Outline each uninfected red blood cell.
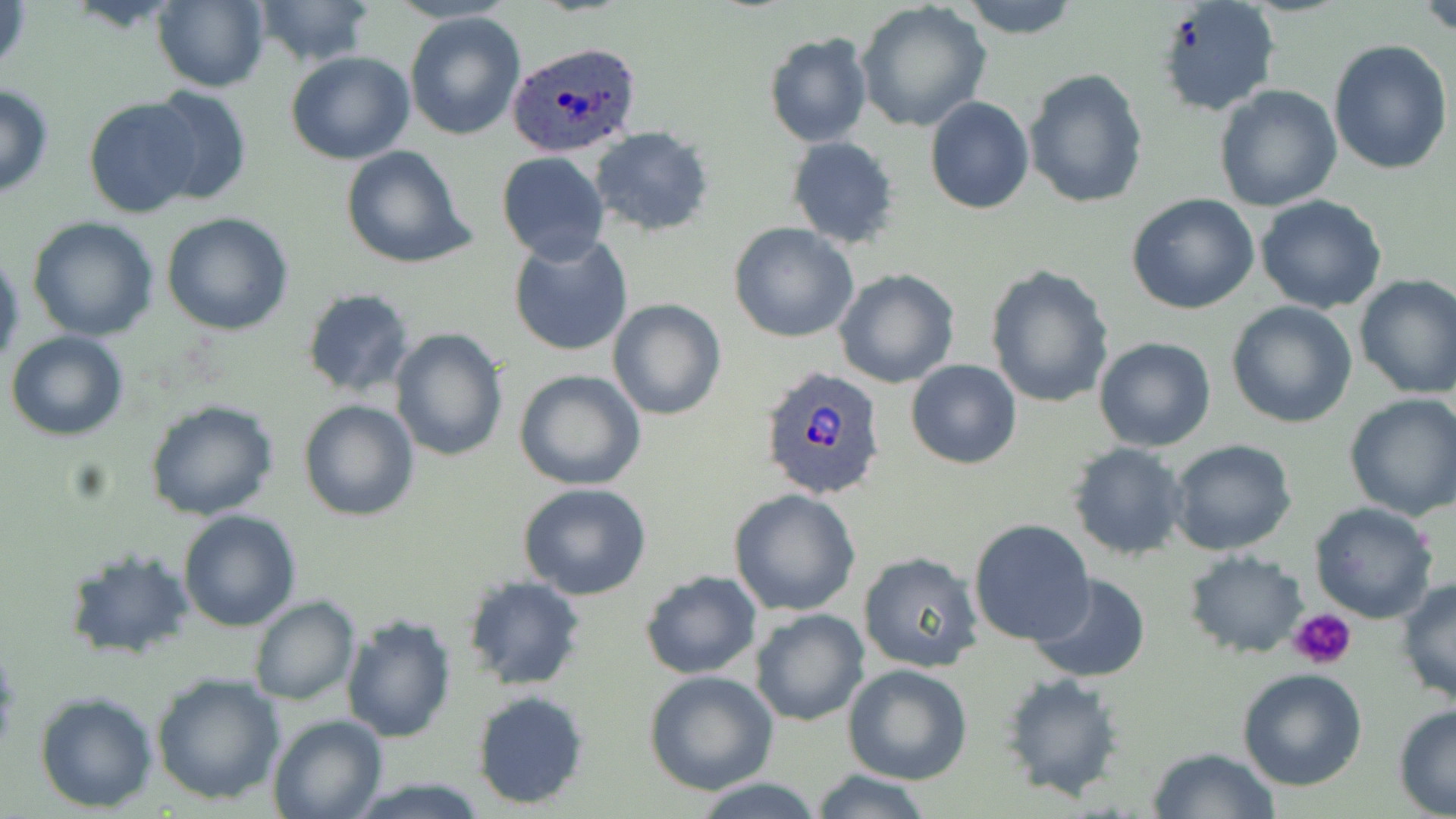

Approximate bounding boxes as named x1/y1/x2/y2 corners in pixels.
Uninfected red blood cells: (x1=1, y1=0, x2=32, y2=82), (x1=152, y1=0, x2=270, y2=92), (x1=956, y1=0, x2=1083, y2=38), (x1=1155, y1=0, x2=1280, y2=115), (x1=1417, y1=0, x2=1456, y2=36), (x1=252, y1=2, x2=375, y2=66), (x1=857, y1=3, x2=992, y2=134), (x1=402, y1=12, x2=526, y2=141), (x1=763, y1=32, x2=874, y2=148), (x1=1328, y1=38, x2=1452, y2=175), (x1=285, y1=51, x2=415, y2=165), (x1=1023, y1=69, x2=1149, y2=210), (x1=0, y1=82, x2=54, y2=199), (x1=1214, y1=84, x2=1343, y2=212), (x1=144, y1=85, x2=252, y2=205), (x1=83, y1=96, x2=204, y2=219), (x1=924, y1=97, x2=1034, y2=215), (x1=588, y1=127, x2=713, y2=238), (x1=786, y1=136, x2=902, y2=250), (x1=340, y1=145, x2=476, y2=270), (x1=496, y1=151, x2=611, y2=264), (x1=1125, y1=192, x2=1261, y2=315), (x1=1254, y1=194, x2=1388, y2=314), (x1=161, y1=211, x2=294, y2=335), (x1=27, y1=217, x2=160, y2=341), (x1=729, y1=223, x2=860, y2=344), (x1=507, y1=234, x2=633, y2=357), (x1=0, y1=249, x2=23, y2=369), (x1=984, y1=264, x2=1115, y2=408), (x1=834, y1=270, x2=960, y2=388), (x1=1353, y1=274, x2=1456, y2=398), (x1=300, y1=288, x2=416, y2=397), (x1=607, y1=299, x2=727, y2=420), (x1=1226, y1=300, x2=1358, y2=428), (x1=388, y1=328, x2=509, y2=463), (x1=6, y1=329, x2=129, y2=441), (x1=1094, y1=337, x2=1218, y2=452), (x1=906, y1=359, x2=1023, y2=469), (x1=513, y1=369, x2=646, y2=491), (x1=1343, y1=393, x2=1456, y2=521), (x1=144, y1=397, x2=279, y2=521), (x1=298, y1=399, x2=420, y2=520), (x1=1167, y1=439, x2=1297, y2=556), (x1=1066, y1=442, x2=1189, y2=562), (x1=518, y1=482, x2=654, y2=601), (x1=729, y1=488, x2=860, y2=616), (x1=1308, y1=502, x2=1439, y2=624), (x1=178, y1=509, x2=302, y2=631), (x1=968, y1=518, x2=1094, y2=644), (x1=66, y1=545, x2=194, y2=661), (x1=1184, y1=550, x2=1309, y2=659), (x1=858, y1=552, x2=984, y2=674), (x1=639, y1=570, x2=763, y2=679), (x1=461, y1=574, x2=588, y2=689), (x1=1026, y1=574, x2=1151, y2=683), (x1=1396, y1=576, x2=1456, y2=709), (x1=249, y1=596, x2=360, y2=706), (x1=751, y1=609, x2=870, y2=727), (x1=340, y1=612, x2=456, y2=743), (x1=842, y1=664, x2=972, y2=785), (x1=1236, y1=668, x2=1368, y2=790), (x1=999, y1=669, x2=1129, y2=801), (x1=150, y1=670, x2=285, y2=805), (x1=645, y1=670, x2=779, y2=795), (x1=470, y1=690, x2=590, y2=811), (x1=34, y1=691, x2=159, y2=812), (x1=1392, y1=704, x2=1456, y2=817), (x1=267, y1=714, x2=386, y2=819), (x1=1146, y1=746, x2=1280, y2=819), (x1=807, y1=767, x2=935, y2=819), (x1=691, y1=778, x2=823, y2=818).

Plasmodium ovale-infected red blood cell locations = approximate bounding boxes as named x1/y1/x2/y2 corners in pixels: (x1=507, y1=41, x2=644, y2=158), (x1=760, y1=368, x2=886, y2=502)
slide-level diagnosis = Plasmodium ovale
magnification = 1000x
field of view = single
platelet locations = approximate bounding boxes as named x1/y1/x2/y2 corners in pixels: (x1=1290, y1=607, x2=1358, y2=670)
image size = 1456×819 pixels
stain = May-Grünwald-Giemsa
preparation = thin blood film
modality = light microscopy